Report the malaria status.
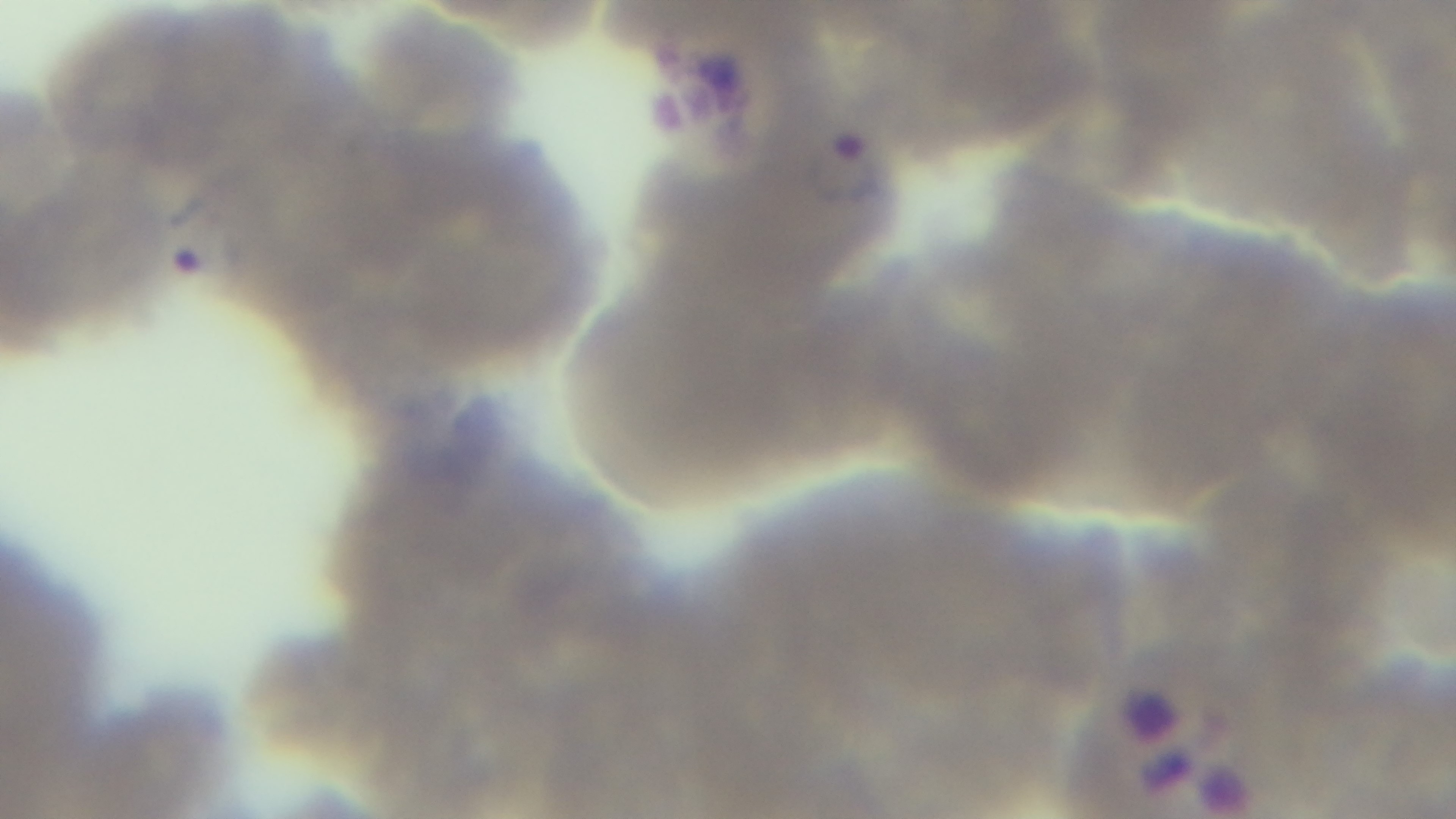

Infected.

objective = 100x oil immersion
stain = Giemsa
field of view = single
capture = mounted 4K digital camera
preparation = thin
modality = light microscopy